Classify this cell by malaria status.
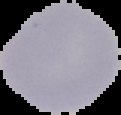

It is uninfected.

{
  "image_size": "121×115 pixels",
  "image_type": "cell region segmented out of the field of view; surrounding area masked to black",
  "preparation": "thin blood smear"
}